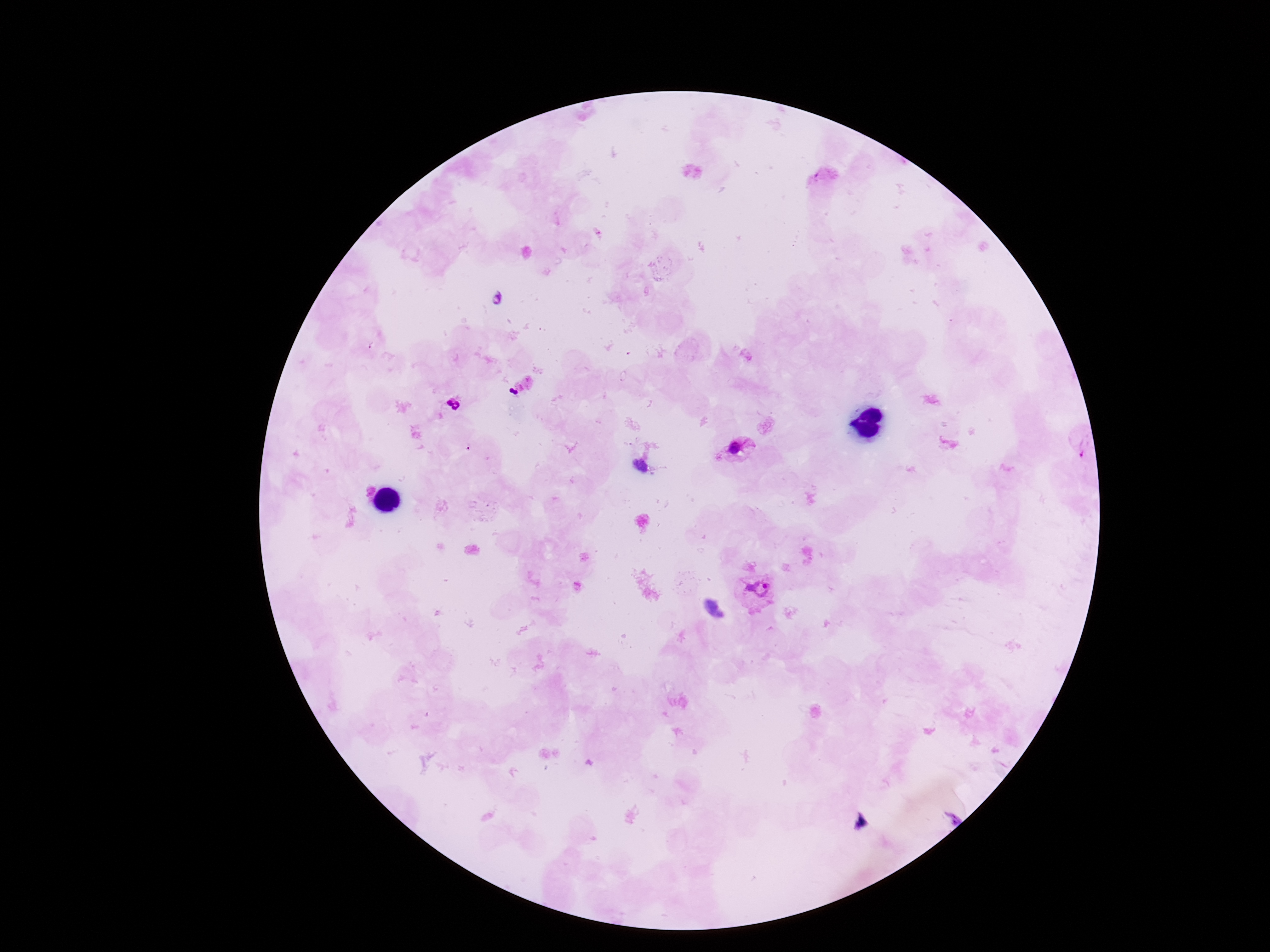
preparation = thick blood smear
magnification = 100x
image size = 1270×952 pixels
capture = smartphone camera through the microscope eyepiece
Plasmodium parasite locations = approximate object centers, in pixels from the top-left corner: (x=454, y=405), (x=737, y=449), (x=760, y=586)
patient malaria status = positive
field of view = single
stain = Giemsa